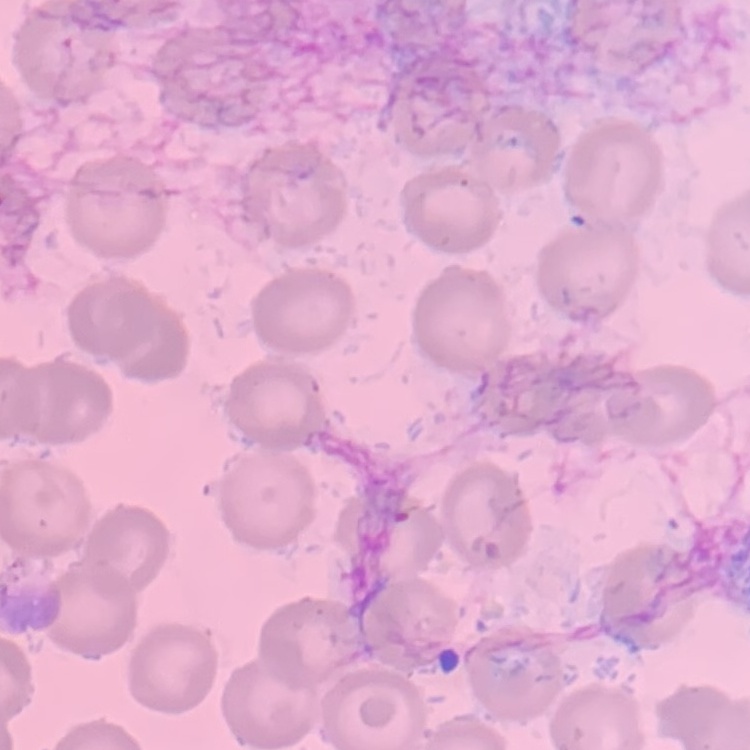

Summary:
  - Red blood cell morphology: no rouleaux formation
  - Image type: one tile cut from a larger photomicrograph
  - Preparation: thin blood film
  - Stain: Field's or Giemsa